State which parasite is depicted.
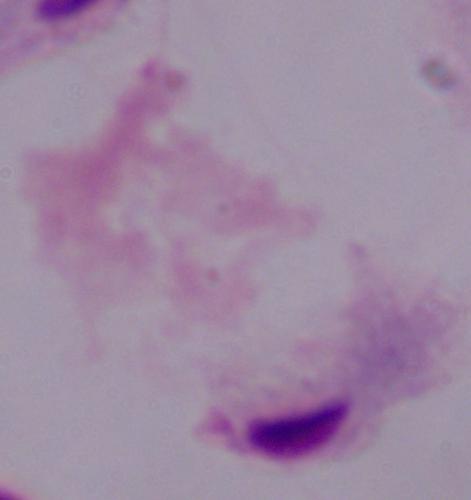
A trichomonad.

Summary:
  - Modality: micrograph
  - Magnification: 1000x